Identify the blood parasite species.
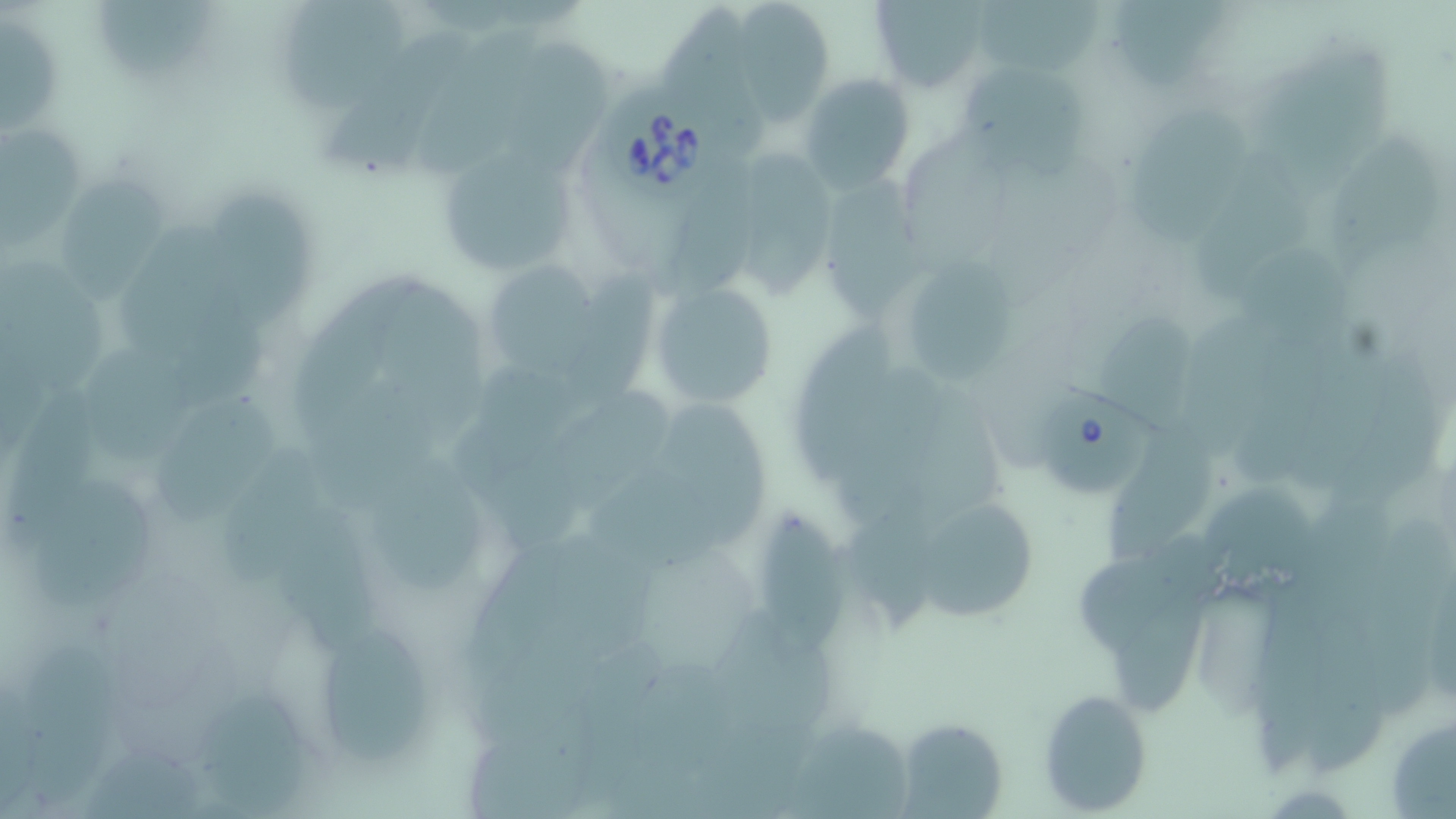
Babesia divergens.

Approximate bounding boxes as (x1,y1)-(x2,y2) corner pairs in pixels. Babesia divergens-infected red blood cell locations: (608,88)-(720,200), (1034,380)-(1158,502). Uninfected red blood cell locations: (282,0)-(413,114), (869,0)-(989,92), (95,1)-(223,76), (738,1)-(831,127), (967,1)-(1112,80), (1111,1)-(1237,89), (660,6)-(774,164), (0,16)-(68,141), (407,22)-(543,187), (513,36)-(612,170), (1270,44)-(1392,193), (964,60)-(1093,175), (800,74)-(915,193), (1129,104)-(1252,238), (0,127)-(81,251), (1329,127)-(1441,284), (429,137)-(579,278), (1198,142)-(1318,301), (742,145)-(845,301), (678,162)-(766,297), (818,167)-(937,322), (56,174)-(171,304), (204,189)-(325,333), (125,236)-(267,402), (1235,242)-(1352,356), (905,258)-(1016,383), (567,261)-(657,408), (492,265)-(598,378), (294,269)-(433,452), (647,274)-(781,410), (381,283)-(484,442), (791,316)-(909,488), (1100,318)-(1195,429), (80,343)-(190,468), (460,371)-(583,520), (509,391)-(674,544), (151,393)-(282,530), (657,406)-(776,547), (1111,417)-(1230,563), (222,444)-(330,585), (371,449)-(489,597), (33,478)-(159,607), (844,487)-(949,640), (921,501)-(1042,618), (757,502)-(847,659), (469,527)-(579,684), (527,528)-(657,673), (1080,541)-(1218,655), (717,609)-(837,742), (324,634)-(438,758), (24,643)-(122,802), (196,686)-(311,816), (1038,688)-(1155,815), (467,694)-(599,819), (1383,707)-(1455,816), (895,717)-(1010,818). 1000x magnification. May-Grünwald-Giemsa stain. One field of a larger specimen. Image is 1456×819 pixels. Light microscopy. Thin blood film.